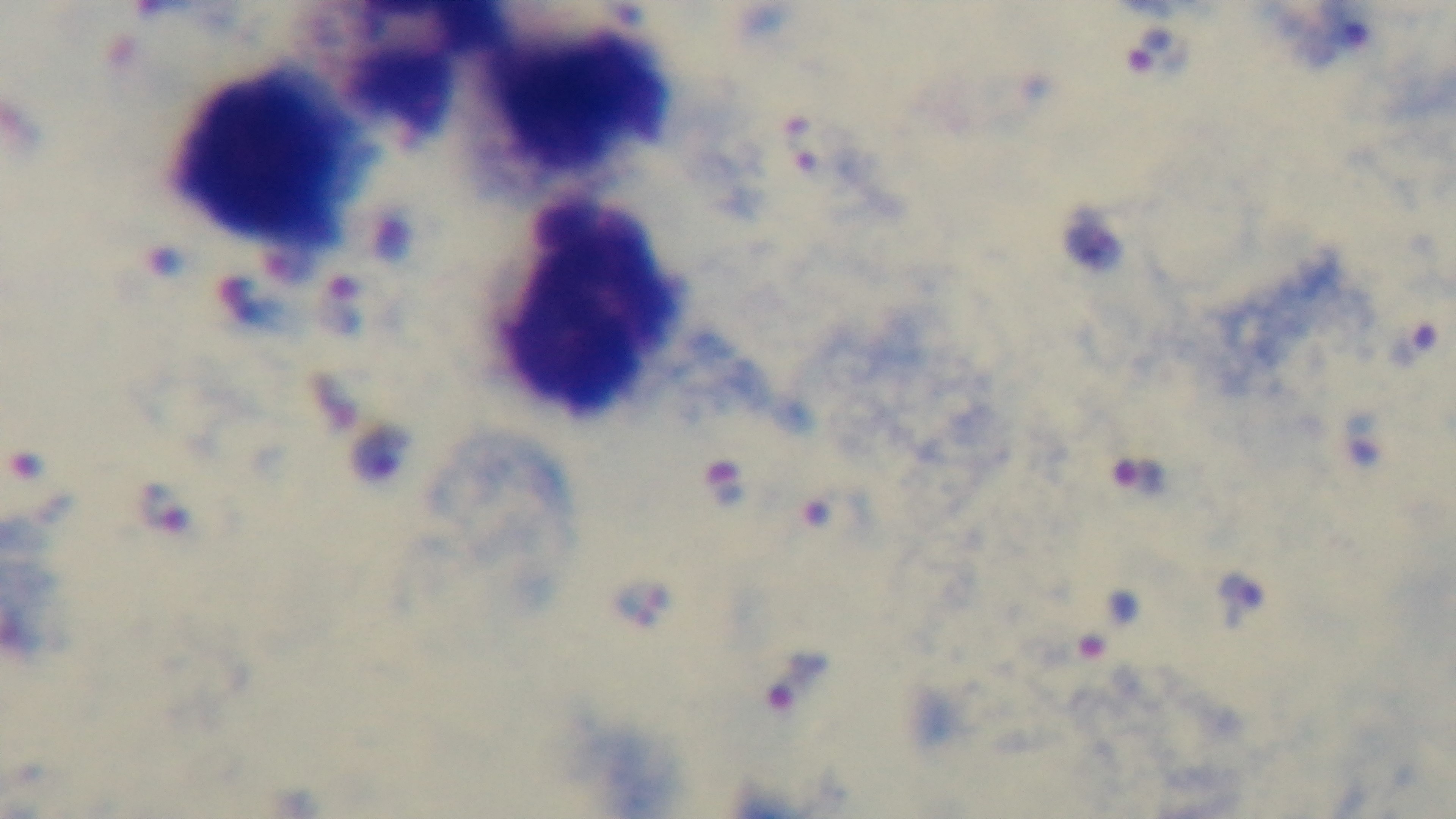

objective: 100x oil immersion
malaria_status: infected
field_of_view: one from the slide
modality: light microscopy
preparation: thick smear
capture: mounted 4K digital camera
stain: Giemsa